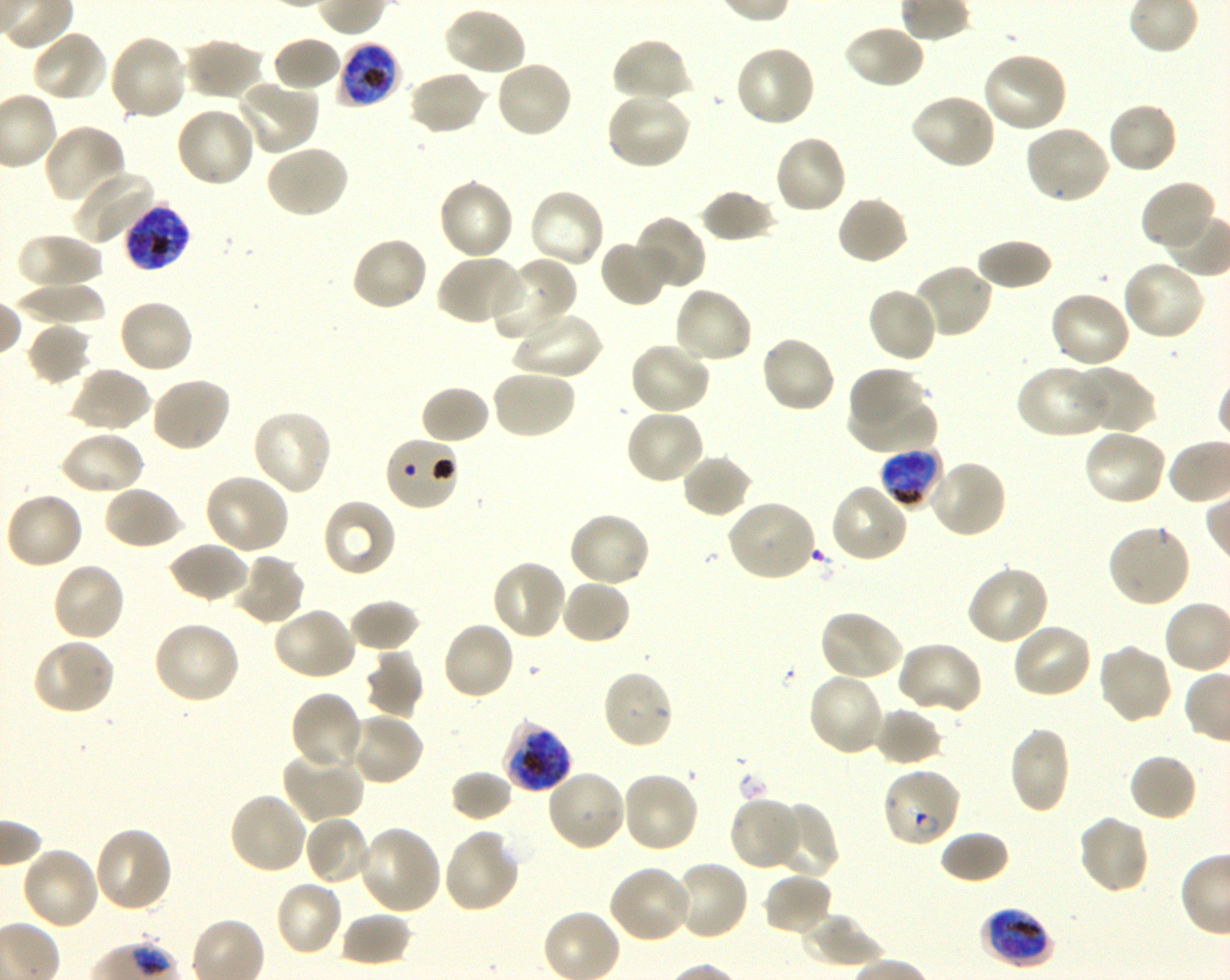

Approximate bounding rectangles given as corner coordinates in pixels from the top-left. Not every red blood cell is marked. A life-cycle stage — or a range of stages, where the recorded stages span more than one — follows each staged infected red blood cell. Locations of uninfected red blood cells: (x1=442, y1=5, x2=527, y2=78), (x1=842, y1=24, x2=926, y2=91), (x1=30, y1=29, x2=110, y2=103), (x1=108, y1=34, x2=188, y2=122), (x1=182, y1=37, x2=265, y2=101), (x1=271, y1=37, x2=343, y2=93), (x1=610, y1=37, x2=692, y2=105), (x1=734, y1=44, x2=817, y2=128), (x1=980, y1=52, x2=1069, y2=135), (x1=494, y1=60, x2=574, y2=140), (x1=407, y1=69, x2=488, y2=137), (x1=234, y1=79, x2=320, y2=156), (x1=604, y1=92, x2=692, y2=172), (x1=909, y1=93, x2=997, y2=171), (x1=1106, y1=101, x2=1178, y2=175), (x1=174, y1=106, x2=257, y2=189), (x1=41, y1=123, x2=126, y2=205), (x1=1023, y1=123, x2=1111, y2=205), (x1=773, y1=133, x2=847, y2=216), (x1=265, y1=143, x2=350, y2=219), (x1=69, y1=169, x2=159, y2=247), (x1=437, y1=177, x2=515, y2=262), (x1=1140, y1=181, x2=1217, y2=252), (x1=699, y1=187, x2=777, y2=243), (x1=526, y1=188, x2=606, y2=271), (x1=835, y1=194, x2=910, y2=266), (x1=632, y1=215, x2=707, y2=292), (x1=17, y1=233, x2=104, y2=295), (x1=349, y1=235, x2=429, y2=313), (x1=975, y1=237, x2=1053, y2=291), (x1=599, y1=238, x2=673, y2=308), (x1=436, y1=253, x2=524, y2=327), (x1=492, y1=257, x2=578, y2=343), (x1=1121, y1=259, x2=1207, y2=341), (x1=908, y1=264, x2=993, y2=340), (x1=13, y1=284, x2=108, y2=326), (x1=672, y1=286, x2=754, y2=366), (x1=865, y1=286, x2=939, y2=364), (x1=1049, y1=290, x2=1133, y2=370), (x1=117, y1=298, x2=194, y2=376), (x1=510, y1=309, x2=602, y2=382), (x1=27, y1=322, x2=93, y2=386), (x1=759, y1=335, x2=838, y2=415), (x1=628, y1=340, x2=712, y2=415), (x1=1015, y1=364, x2=1110, y2=439), (x1=68, y1=365, x2=152, y2=433), (x1=848, y1=366, x2=925, y2=430), (x1=1073, y1=367, x2=1157, y2=435), (x1=490, y1=368, x2=576, y2=440), (x1=150, y1=375, x2=232, y2=453), (x1=419, y1=384, x2=492, y2=445), (x1=848, y1=396, x2=937, y2=453), (x1=623, y1=407, x2=707, y2=486), (x1=250, y1=408, x2=334, y2=497), (x1=1082, y1=427, x2=1168, y2=507), (x1=58, y1=430, x2=145, y2=496), (x1=680, y1=453, x2=754, y2=519), (x1=925, y1=459, x2=1007, y2=539), (x1=203, y1=473, x2=291, y2=554), (x1=828, y1=483, x2=910, y2=564), (x1=103, y1=484, x2=183, y2=550), (x1=3, y1=491, x2=84, y2=571), (x1=321, y1=497, x2=397, y2=579), (x1=724, y1=499, x2=817, y2=583), (x1=567, y1=511, x2=653, y2=588), (x1=1107, y1=522, x2=1192, y2=608), (x1=168, y1=541, x2=249, y2=604), (x1=231, y1=553, x2=308, y2=627), (x1=490, y1=559, x2=567, y2=641), (x1=50, y1=561, x2=127, y2=642), (x1=966, y1=564, x2=1051, y2=646), (x1=560, y1=579, x2=632, y2=646), (x1=349, y1=598, x2=421, y2=653), (x1=271, y1=605, x2=358, y2=681), (x1=818, y1=609, x2=905, y2=683), (x1=152, y1=621, x2=242, y2=705), (x1=441, y1=621, x2=516, y2=701), (x1=1011, y1=622, x2=1093, y2=700), (x1=31, y1=638, x2=117, y2=716), (x1=895, y1=641, x2=984, y2=718), (x1=1096, y1=642, x2=1174, y2=727), (x1=364, y1=650, x2=425, y2=720), (x1=602, y1=668, x2=676, y2=750), (x1=806, y1=672, x2=885, y2=757), (x1=290, y1=691, x2=365, y2=773), (x1=873, y1=708, x2=945, y2=767), (x1=348, y1=710, x2=425, y2=787), (x1=1007, y1=727, x2=1071, y2=814), (x1=281, y1=748, x2=366, y2=824), (x1=1128, y1=753, x2=1199, y2=823), (x1=545, y1=768, x2=626, y2=852), (x1=450, y1=769, x2=514, y2=823), (x1=621, y1=770, x2=701, y2=854), (x1=228, y1=791, x2=309, y2=876), (x1=728, y1=795, x2=803, y2=871), (x1=768, y1=801, x2=838, y2=879), (x1=303, y1=814, x2=374, y2=887), (x1=1075, y1=814, x2=1151, y2=896), (x1=93, y1=825, x2=173, y2=913), (x1=358, y1=825, x2=442, y2=916), (x1=442, y1=828, x2=522, y2=914), (x1=939, y1=830, x2=1011, y2=885), (x1=20, y1=845, x2=102, y2=931), (x1=673, y1=859, x2=750, y2=941), (x1=607, y1=865, x2=694, y2=944), (x1=761, y1=872, x2=834, y2=937), (x1=274, y1=879, x2=345, y2=958), (x1=340, y1=911, x2=414, y2=967), (x1=802, y1=912, x2=884, y2=969). Locations of red blood cells of indeterminate infection status: (x1=383, y1=436, x2=462, y2=512). Locations of infected red blood cells: (x1=337, y1=40, x2=400, y2=106) late trophozoite to late schizont; (x1=122, y1=203, x2=191, y2=274) late trophozoite to late schizont; (x1=880, y1=447, x2=943, y2=507) late trophozoite to early schizont; (x1=500, y1=719, x2=572, y2=793) late trophozoite to late schizont; (x1=881, y1=766, x2=962, y2=849) ring; (x1=980, y1=908, x2=1053, y2=968) late trophozoite to early schizont. One field from this slide. 100x oil-immersion objective, numerical aperture 1.30. Giemsa-stained preparation. Donor blood group O+. Shaking in-vitro culture of Plasmodium falciparum strain 3D7. Image is 1230×980 pixels. Thin blood smear.